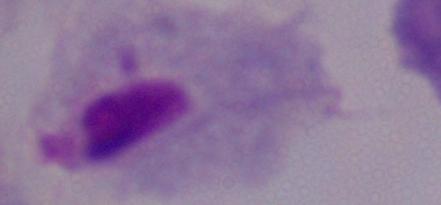
Micrograph. A trichomonad is seen. 1000x magnification.